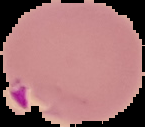 Cell region segmented out of the field of view; the surrounding area is masked to black. From a thin blood smear. Image is 145×127 pixels. Malaria status: parasitized.